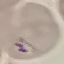

Summary:
  - Result: malaria parasites detected
  - Stain: Giemsa
  - Image type: automatically extracted cell patch, resized to 64 × 64 pixels
  - Capture: smartphone camera at the microscope eyepiece
  - Preparation: thin blood film